State which parasite is depicted.
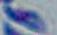
Toxoplasma gondii.

1000x magnification. Micrograph.